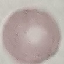

malaria status = uninfected
preparation = thin smear
stain = Giemsa
image type = automatically extracted cell patch, resized to 64 × 64 pixels
capture = smartphone camera at the microscope eyepiece